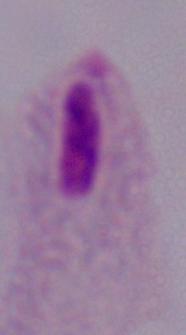

magnification = 1000x
modality = photomicrograph
identification = trichomonad